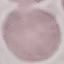
result = negative for malaria parasites
preparation = thin smear
stain = Giemsa
image type = automatically extracted cell patch, resized to 64 × 64 pixels
capture = smartphone through the microscope eyepiece